Locate every blood parasite and identify its species.
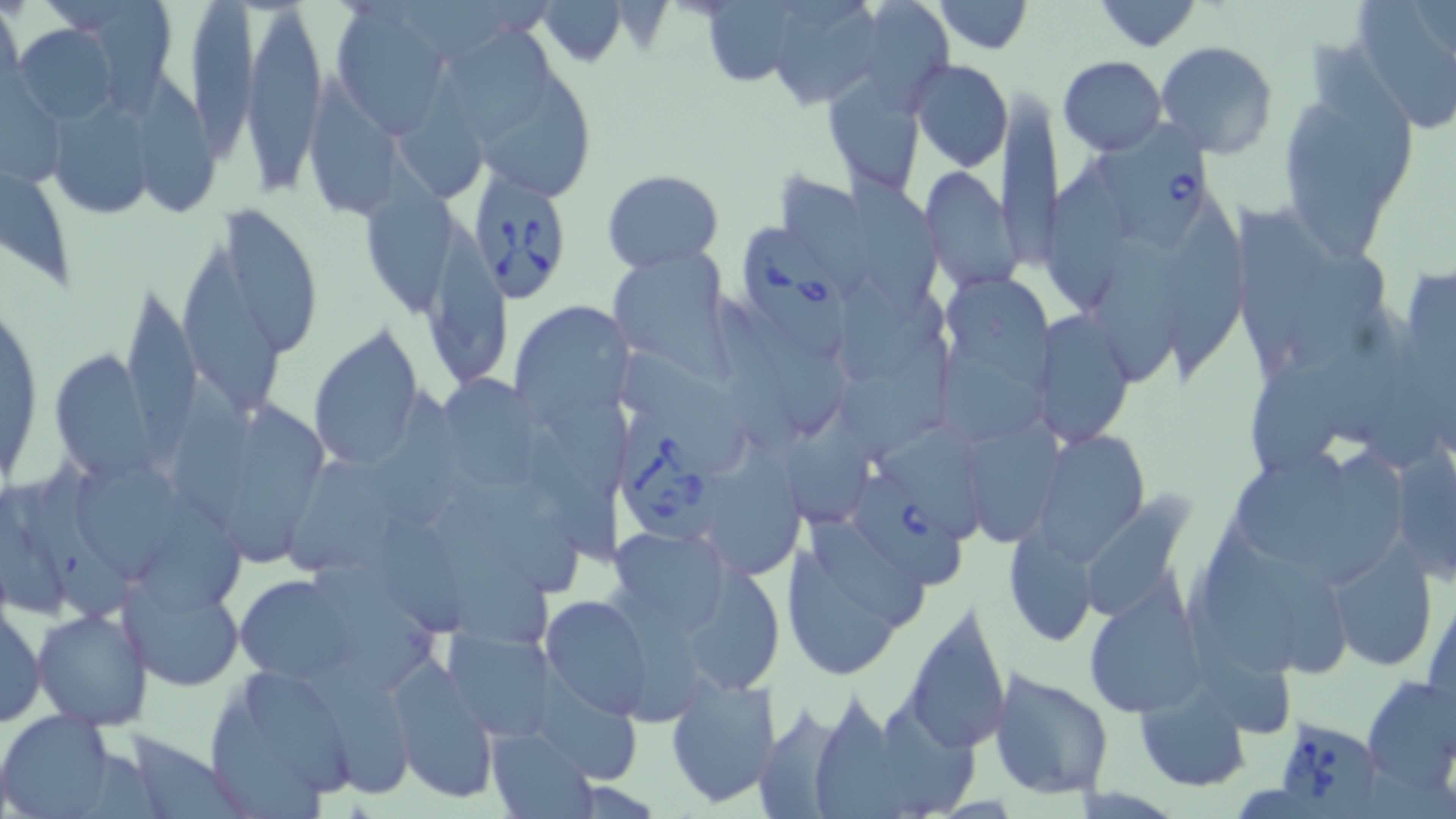
Approximate bounding boxes as named x1/y1/x2/y2 corners in pixels.
Babesia divergens-infected red blood cells: (x1=1096, y1=111, x2=1216, y2=254), (x1=468, y1=165, x2=575, y2=306), (x1=742, y1=225, x2=852, y2=362), (x1=621, y1=411, x2=724, y2=546), (x1=855, y1=470, x2=966, y2=586), (x1=1270, y1=715, x2=1384, y2=815).
No Plasmodium falciparum, Plasmodium ovale, Plasmodium malariae, Plasmodium vivax, or Trypanosoma brucei observed.

Uninfected red blood cell locations: (x1=0, y1=0, x2=24, y2=103), (x1=329, y1=0, x2=458, y2=133), (x1=934, y1=0, x2=1032, y2=54), (x1=1091, y1=0, x2=1202, y2=51), (x1=94, y1=1, x2=175, y2=115), (x1=192, y1=1, x2=263, y2=161), (x1=412, y1=1, x2=516, y2=63), (x1=251, y1=3, x2=321, y2=196), (x1=1351, y1=3, x2=1455, y2=134), (x1=454, y1=20, x2=551, y2=147), (x1=12, y1=21, x2=124, y2=124), (x1=1155, y1=40, x2=1279, y2=159), (x1=1057, y1=56, x2=1168, y2=155), (x1=909, y1=58, x2=1012, y2=171), (x1=401, y1=64, x2=485, y2=200), (x1=481, y1=64, x2=595, y2=200), (x1=311, y1=71, x2=406, y2=225), (x1=144, y1=72, x2=217, y2=218), (x1=1276, y1=72, x2=1420, y2=256), (x1=826, y1=73, x2=928, y2=196), (x1=0, y1=76, x2=68, y2=193), (x1=997, y1=91, x2=1062, y2=269), (x1=54, y1=95, x2=157, y2=215), (x1=366, y1=149, x2=460, y2=318), (x1=1046, y1=157, x2=1132, y2=312), (x1=920, y1=164, x2=1022, y2=294), (x1=849, y1=165, x2=951, y2=328), (x1=601, y1=168, x2=725, y2=271), (x1=0, y1=170, x2=79, y2=295), (x1=779, y1=170, x2=868, y2=299), (x1=1164, y1=194, x2=1245, y2=378), (x1=1238, y1=202, x2=1325, y2=365), (x1=221, y1=205, x2=321, y2=357), (x1=427, y1=216, x2=507, y2=383), (x1=1095, y1=235, x2=1185, y2=387), (x1=184, y1=241, x2=283, y2=412), (x1=1281, y1=243, x2=1394, y2=377), (x1=606, y1=249, x2=731, y2=370), (x1=1400, y1=264, x2=1455, y2=373), (x1=942, y1=276, x2=1055, y2=394), (x1=843, y1=281, x2=947, y2=384), (x1=1, y1=287, x2=45, y2=495), (x1=124, y1=288, x2=200, y2=467), (x1=731, y1=300, x2=848, y2=434), (x1=508, y1=302, x2=632, y2=424), (x1=1035, y1=311, x2=1135, y2=447), (x1=309, y1=327, x2=423, y2=472), (x1=940, y1=343, x2=1049, y2=449), (x1=1247, y1=348, x2=1343, y2=478), (x1=621, y1=349, x2=752, y2=472), (x1=843, y1=349, x2=956, y2=463), (x1=48, y1=351, x2=158, y2=485), (x1=167, y1=369, x2=268, y2=532), (x1=444, y1=372, x2=547, y2=494), (x1=376, y1=387, x2=471, y2=527), (x1=223, y1=393, x2=332, y2=560), (x1=544, y1=395, x2=639, y2=498), (x1=787, y1=417, x2=873, y2=524), (x1=966, y1=418, x2=1064, y2=546), (x1=528, y1=424, x2=623, y2=567), (x1=885, y1=426, x2=980, y2=539), (x1=1031, y1=429, x2=1151, y2=562), (x1=711, y1=442, x2=807, y2=580), (x1=1388, y1=443, x2=1456, y2=581), (x1=1317, y1=446, x2=1408, y2=584), (x1=280, y1=448, x2=396, y2=574), (x1=1236, y1=452, x2=1354, y2=557), (x1=17, y1=455, x2=142, y2=622), (x1=80, y1=462, x2=191, y2=584), (x1=450, y1=475, x2=580, y2=594), (x1=140, y1=491, x2=249, y2=618), (x1=1083, y1=499, x2=1194, y2=618), (x1=382, y1=514, x2=463, y2=639), (x1=806, y1=516, x2=930, y2=626), (x1=430, y1=518, x2=554, y2=645), (x1=1197, y1=520, x2=1305, y2=683), (x1=1004, y1=528, x2=1098, y2=644), (x1=606, y1=534, x2=727, y2=637), (x1=778, y1=542, x2=930, y2=684), (x1=1254, y1=545, x2=1352, y2=679), (x1=1327, y1=549, x2=1437, y2=671), (x1=314, y1=559, x2=436, y2=695), (x1=121, y1=564, x2=245, y2=692), (x1=687, y1=568, x2=785, y2=696), (x1=236, y1=572, x2=354, y2=681), (x1=610, y1=585, x2=710, y2=728), (x1=1424, y1=586, x2=1456, y2=717), (x1=1086, y1=591, x2=1208, y2=717), (x1=539, y1=593, x2=656, y2=718), (x1=0, y1=597, x2=46, y2=730), (x1=900, y1=600, x2=1012, y2=755), (x1=1187, y1=600, x2=1296, y2=737), (x1=33, y1=607, x2=154, y2=729), (x1=442, y1=628, x2=559, y2=740), (x1=391, y1=661, x2=497, y2=804), (x1=315, y1=663, x2=412, y2=800), (x1=987, y1=665, x2=1114, y2=800), (x1=202, y1=666, x2=358, y2=813), (x1=535, y1=666, x2=645, y2=785), (x1=664, y1=672, x2=779, y2=808), (x1=1359, y1=675, x2=1455, y2=792), (x1=1135, y1=685, x2=1251, y2=790), (x1=813, y1=691, x2=905, y2=819), (x1=882, y1=695, x2=986, y2=819), (x1=758, y1=705, x2=848, y2=819), (x1=0, y1=710, x2=120, y2=817), (x1=486, y1=727, x2=596, y2=817), (x1=111, y1=729, x2=249, y2=819). Slide-level diagnosis: Babesia divergens. Single field of view. Image is 1456×819 pixels. Light microscopy. Thin blood smear. Captured at 1000x magnification. May-Grünwald-Giemsa-stained preparation.